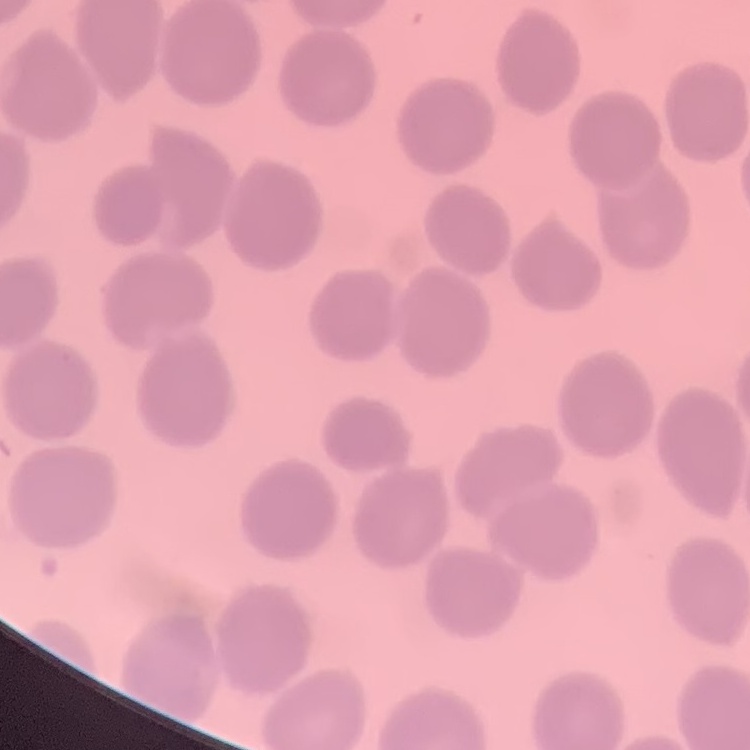

Summary:
  - Red blood cell morphology: no rouleaux formation
  - Preparation: thin peripheral smear
  - Image type: one tile cut from a larger photomicrograph
  - Stain: Field's or Giemsa